Give the position of every Plasmodium parasite.
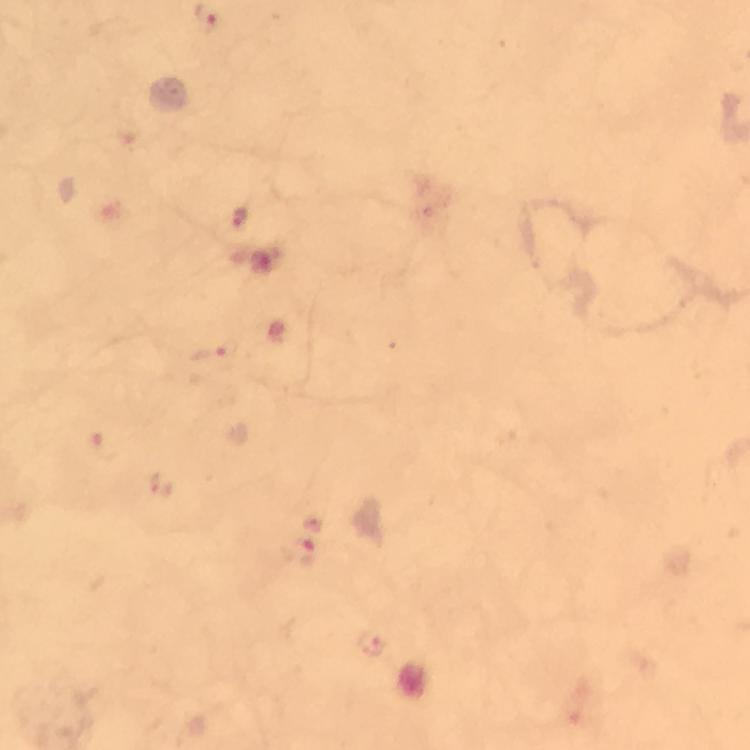

Approximate centers as (x, y) in pixels.
Plasmodium parasites: (238, 215), (103, 443), (162, 488), (300, 551), (371, 642).

Giemsa-stained preparation. Image is 750×750 pixels. Photographed through the microscope with a smartphone camera. From a diagnostic examination for malaria. Thick blood film. 100x magnification. Immersion oil was used. Cropped region of a single field of view.